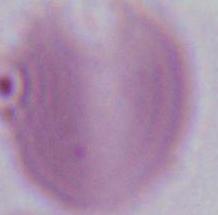
Summary:
  - Magnification: 1000x
  - Modality: photomicrograph
  - Identification: erythrocyte